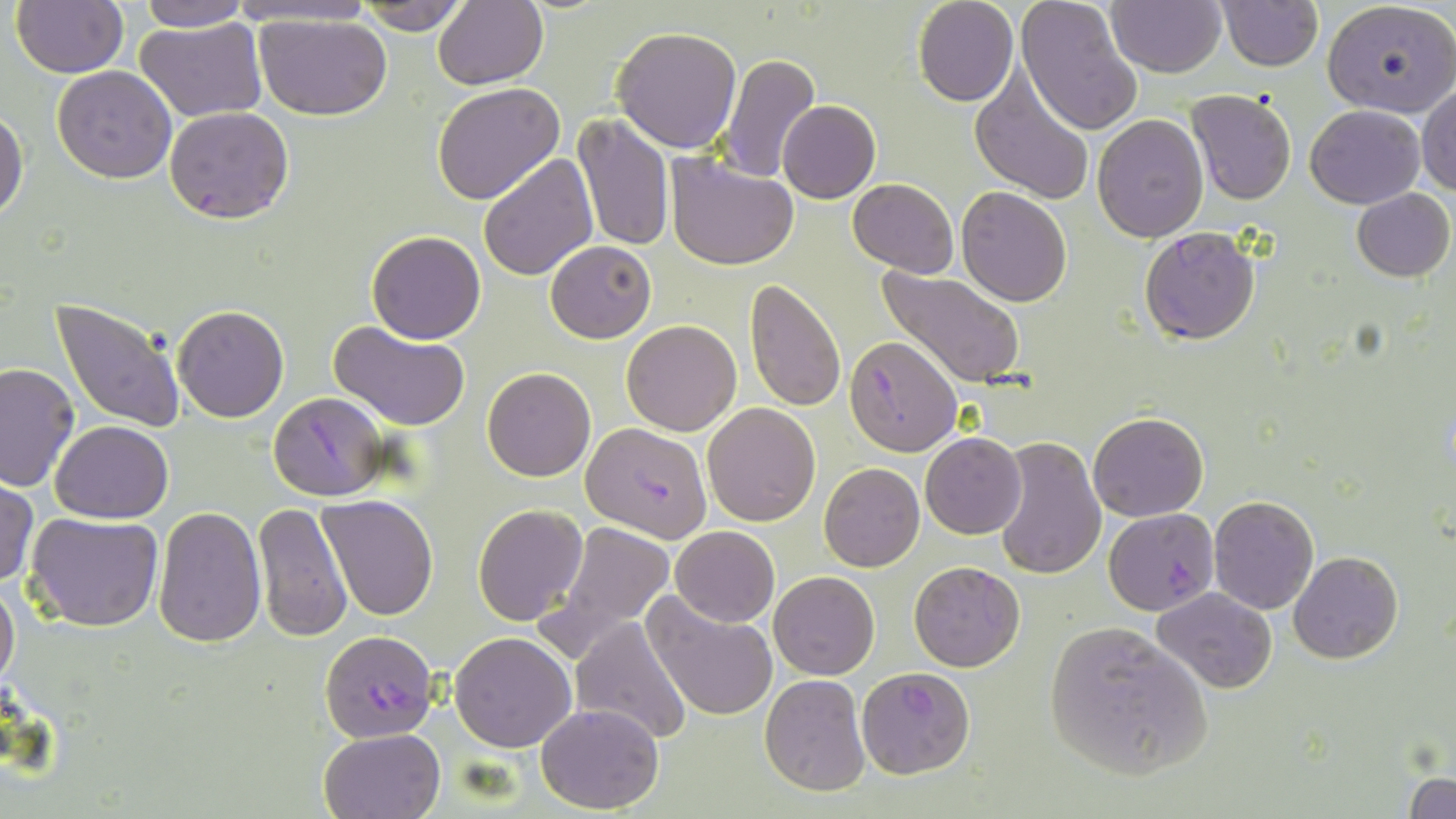

Summary:
  - Coordinate format: approximate bounding boxes as (x1, y1, x2, y2) in pixels
  - Plasmodium falciparum-infected red blood cell locations: (1139, 227, 1261, 345), (844, 337, 960, 455), (268, 391, 388, 500), (580, 420, 713, 541), (1103, 508, 1220, 615), (320, 630, 439, 742), (854, 665, 976, 779)
  - Uninfected red blood cell locations: (9, 0, 128, 78), (229, 0, 379, 29), (912, 0, 1018, 106), (1017, 0, 1145, 136), (1106, 0, 1226, 77), (1216, 0, 1323, 71), (1322, 0, 1456, 118), (135, 1, 252, 31), (355, 2, 470, 35), (432, 2, 548, 89), (254, 11, 394, 122), (137, 15, 267, 122), (612, 24, 743, 152), (717, 53, 821, 182), (52, 66, 178, 183), (970, 68, 1096, 207), (431, 81, 565, 204), (1417, 84, 1456, 196), (1187, 90, 1299, 206), (777, 100, 880, 203), (1306, 104, 1425, 208), (164, 107, 294, 224), (0, 108, 29, 224), (573, 113, 675, 254), (1093, 114, 1209, 242), (479, 152, 598, 280), (664, 152, 799, 270), (847, 178, 959, 277), (955, 186, 1072, 307), (1352, 187, 1454, 281), (367, 230, 486, 343), (545, 240, 656, 343), (878, 266, 1028, 390), (743, 279, 847, 413), (51, 297, 186, 434), (173, 306, 289, 422), (329, 320, 471, 430), (622, 320, 742, 436), (0, 362, 81, 493), (482, 366, 596, 481), (702, 403, 821, 526), (1088, 411, 1208, 522), (51, 420, 173, 523), (921, 432, 1026, 539), (991, 435, 1106, 581), (819, 463, 925, 571), (0, 479, 39, 586), (317, 495, 441, 622), (1208, 496, 1318, 614), (254, 501, 353, 642), (473, 504, 589, 625), (153, 507, 267, 649), (25, 510, 165, 633), (545, 516, 679, 651), (671, 526, 779, 627), (1287, 550, 1403, 664), (909, 560, 1026, 672), (769, 571, 879, 679), (0, 575, 20, 692), (1152, 587, 1276, 694), (644, 591, 779, 722), (568, 617, 692, 745), (1044, 620, 1212, 782), (449, 632, 576, 752), (759, 674, 869, 796), (535, 702, 664, 814), (320, 728, 444, 819), (1407, 773, 1455, 818)
  - Slide-level diagnosis: Plasmodium falciparum
  - Stain: May-Grünwald-Giemsa
  - Modality: optical microscopy
  - Magnification: 1000x
  - Image size: 1456×819 pixels
  - Field of view: single
  - Preparation: thin blood smear